Classify this cell by malaria status.
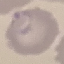
It is parasitized.

capture: smartphone through the microscope eyepiece
stain: Giemsa
image_type: cell patch, automatically extracted from a larger field of view and resized to 64 × 64 pixels
preparation: thin blood smear